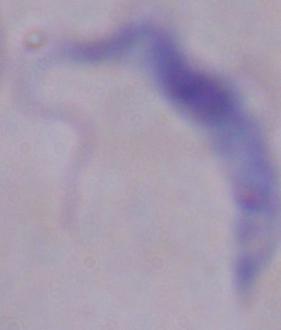

Micrograph. A trypanosome is seen. Captured at 1000x magnification.